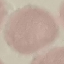

Summary:
  - Malaria status: uninfected
  - Stain: Giemsa
  - Preparation: thin blood smear
  - Image type: automatically extracted cell patch, resized to 64 × 64 pixels
  - Capture: smartphone camera at the microscope eyepiece